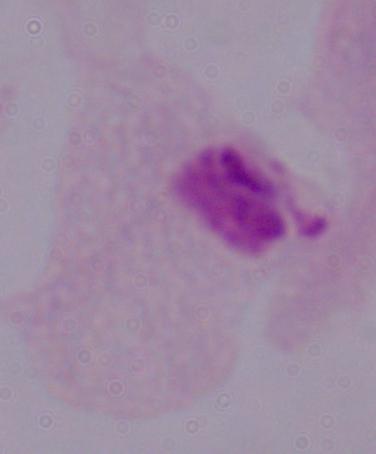
magnification: 1000x
identification: trichomonad
modality: photomicrograph